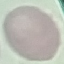
result = negative for malaria parasites
image type = cell patch, automatically extracted from a larger field of view and resized to 64 × 64 pixels
preparation = thin smear
capture = smartphone through the microscope eyepiece
stain = Giemsa